State the preparation type.
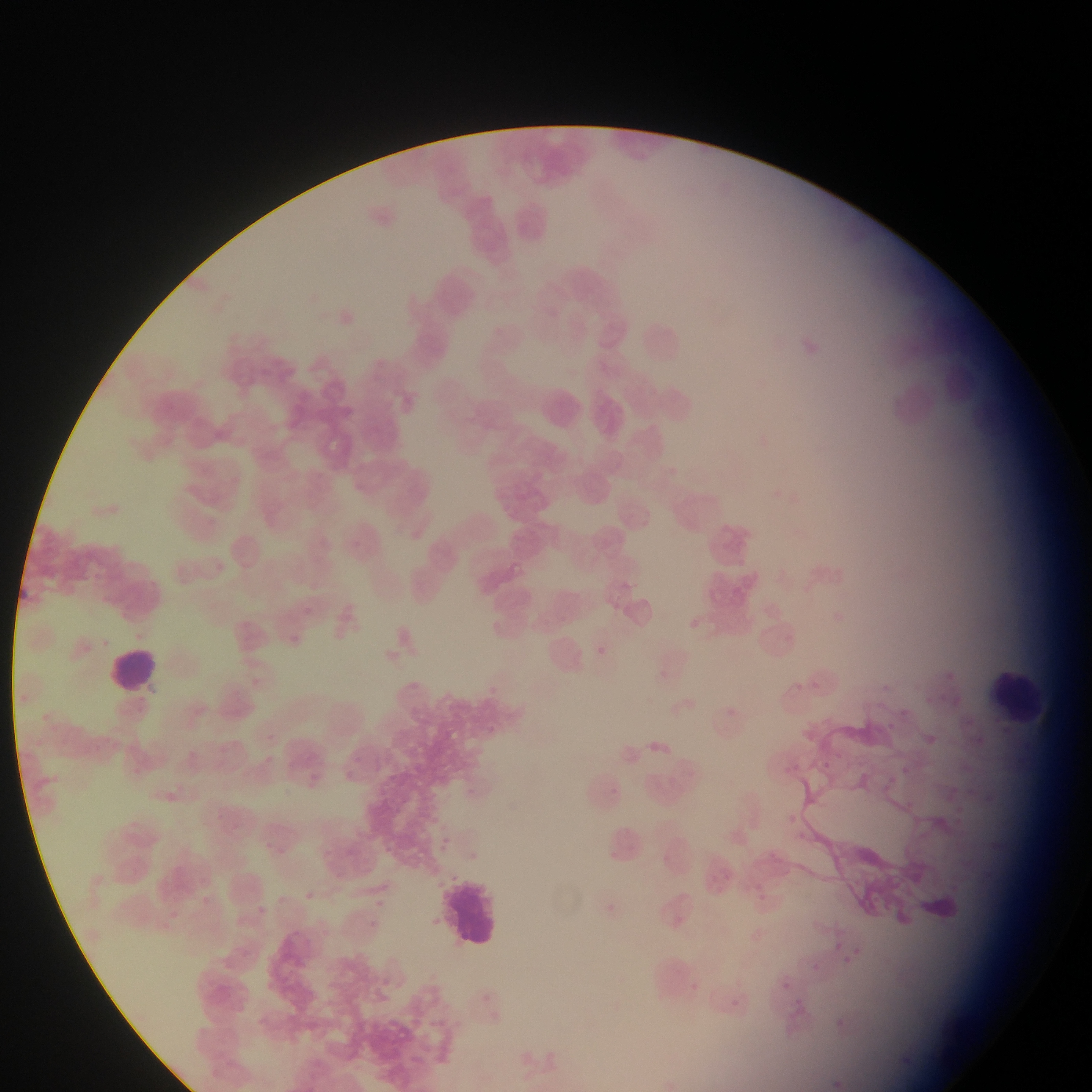

Thin blood smear.

Approximate bounding boxes as (left, top, right, bottom) in pixels.
Summary:
  - Malaria parasite locations: (611, 599, 620, 609), (686, 618, 702, 630), (782, 630, 804, 646), (590, 641, 608, 661), (944, 668, 953, 680), (485, 676, 507, 695), (812, 677, 827, 692), (899, 704, 910, 718), (724, 705, 744, 719), (964, 715, 978, 735), (884, 720, 894, 727), (485, 723, 503, 734), (920, 734, 936, 748), (819, 756, 833, 766), (787, 759, 808, 777), (903, 765, 915, 781), (882, 779, 899, 797), (603, 781, 623, 803), (984, 789, 1000, 803), (949, 802, 966, 816), (781, 807, 798, 826), (797, 830, 813, 845), (756, 879, 766, 889), (751, 886, 764, 906), (831, 938, 845, 952), (840, 944, 864, 967), (809, 961, 823, 975), (775, 975, 794, 992), (686, 978, 702, 991), (731, 998, 740, 1008), (832, 1018, 846, 1025), (903, 1054, 920, 1069), (831, 1075, 848, 1091)
  - Leukocyte locations: (630, 315, 692, 370), (536, 385, 589, 438), (104, 645, 163, 697), (993, 662, 1044, 728), (440, 871, 506, 956)
  - Image size: 1092×1092 pixels
  - Field of view: single
  - Country: Ghana
  - Capture: mobile-phone photograph through a microscope